Name the parasite shown.
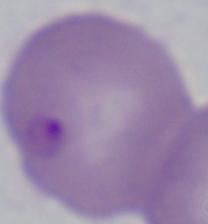
This is Babesia.

Summary:
  - Modality: photomicrograph
  - Magnification: 1000x